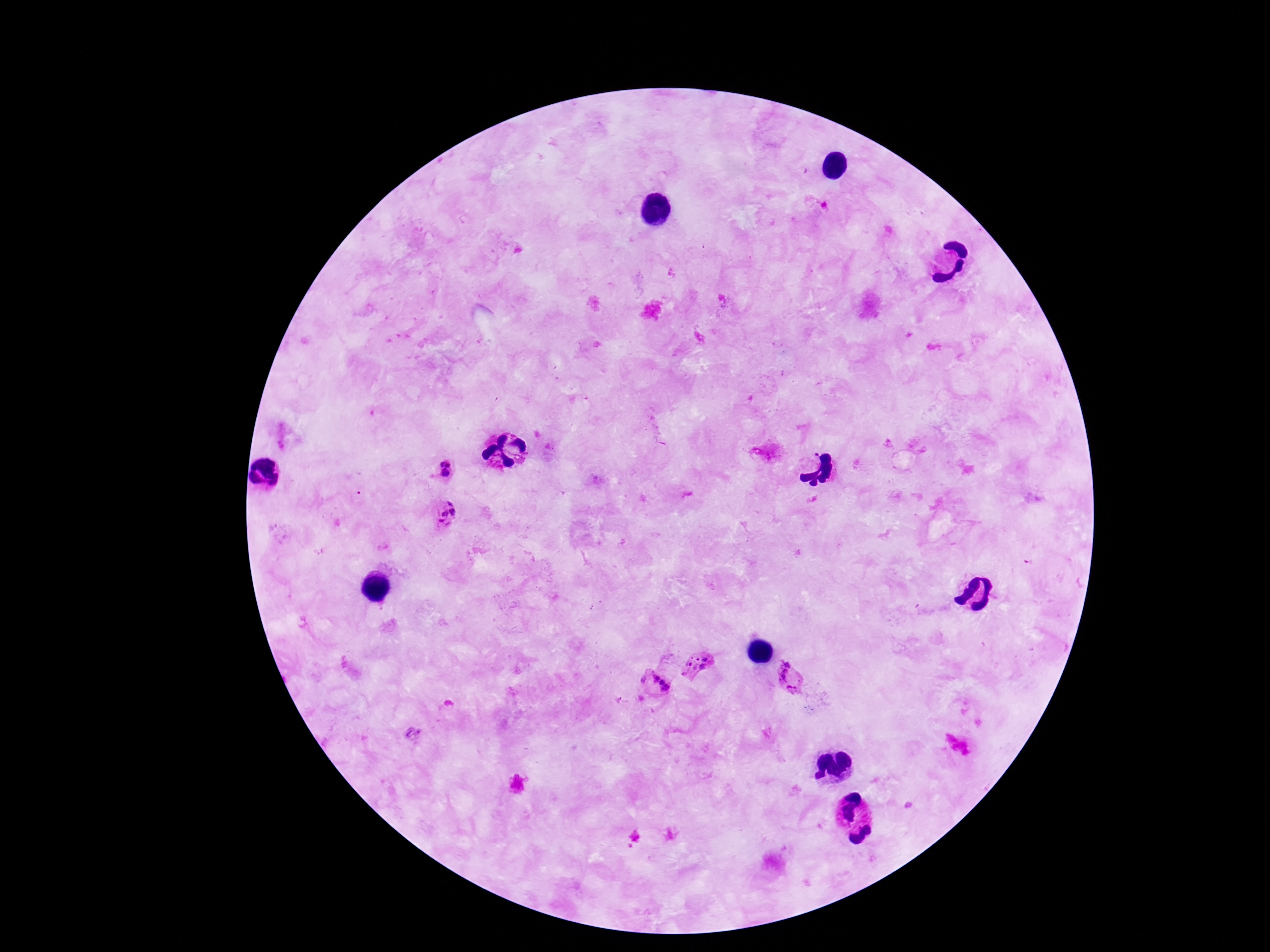

{
  "patient_malaria_status": "infected",
  "stain": "Giemsa",
  "plasmodium_parasite_locations": "approximate centers as [x, y] in pixels: [441, 464], [449, 464], [444, 473], [450, 502], [453, 512], [443, 514], [442, 524], [705, 659], [691, 660], [786, 663], [703, 667], [685, 672], [783, 676], [645, 677], [655, 678], [663, 682], [667, 689], [791, 689]",
  "image_size": "1270×952 pixels",
  "field_of_view": "one from this slide",
  "magnification": "100x",
  "capture": "smartphone camera through the microscope eyepiece",
  "preparation": "thick blood film"
}